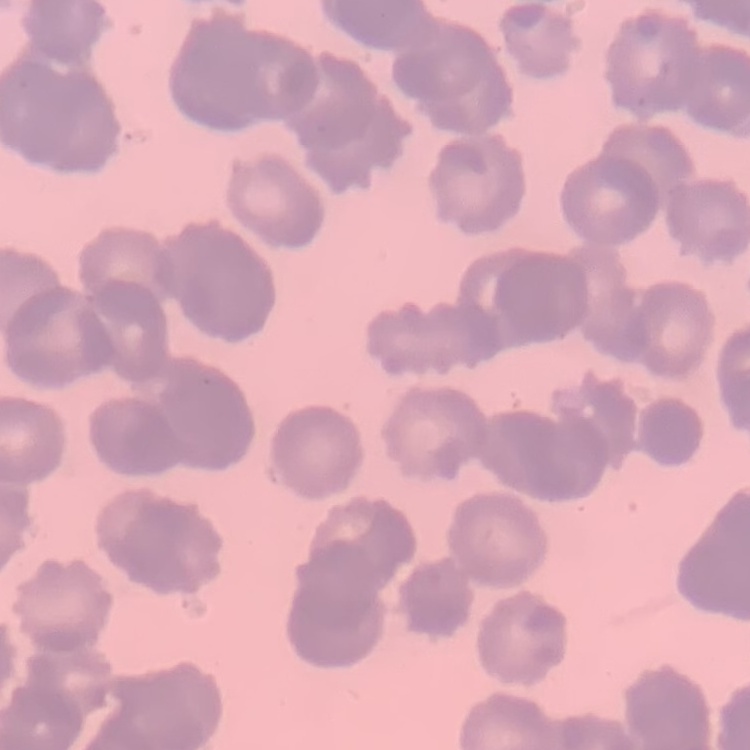
The red blood cells exhibit rouleaux formation. Thin blood smear. Field's or Giemsa stain. Square crop of a larger photomicrograph.